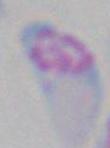
Summary:
  - Magnification: 1000x
  - Modality: micrograph
  - Identification: Toxoplasma gondii